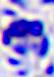

Summary:
  - Magnification: 400x
  - Identification: white blood cell
  - Modality: photomicrograph